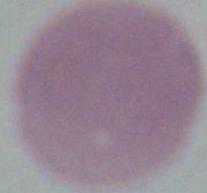
Summary:
  - Magnification: 1000x
  - Modality: micrograph
  - Identification: erythrocyte